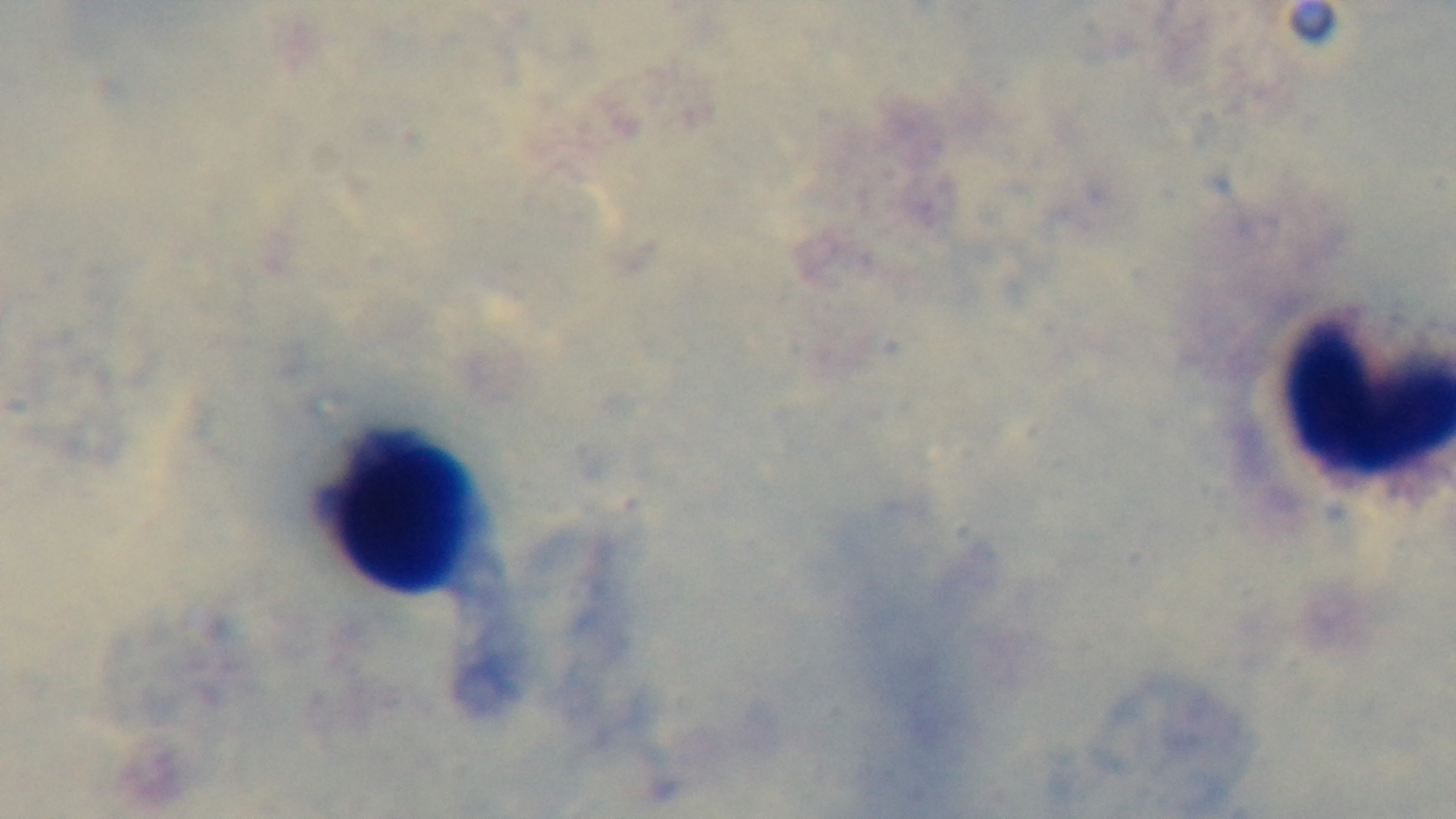

preparation = thick
malaria status = negative
objective = 100x oil immersion
stain = Giemsa
capture = mounted 4K digital camera
modality = light microscopy
field of view = single